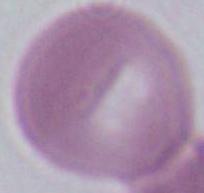

Captured at 1000x magnification. Photomicrograph. A red blood cell is shown.